Point out each malaria parasite.
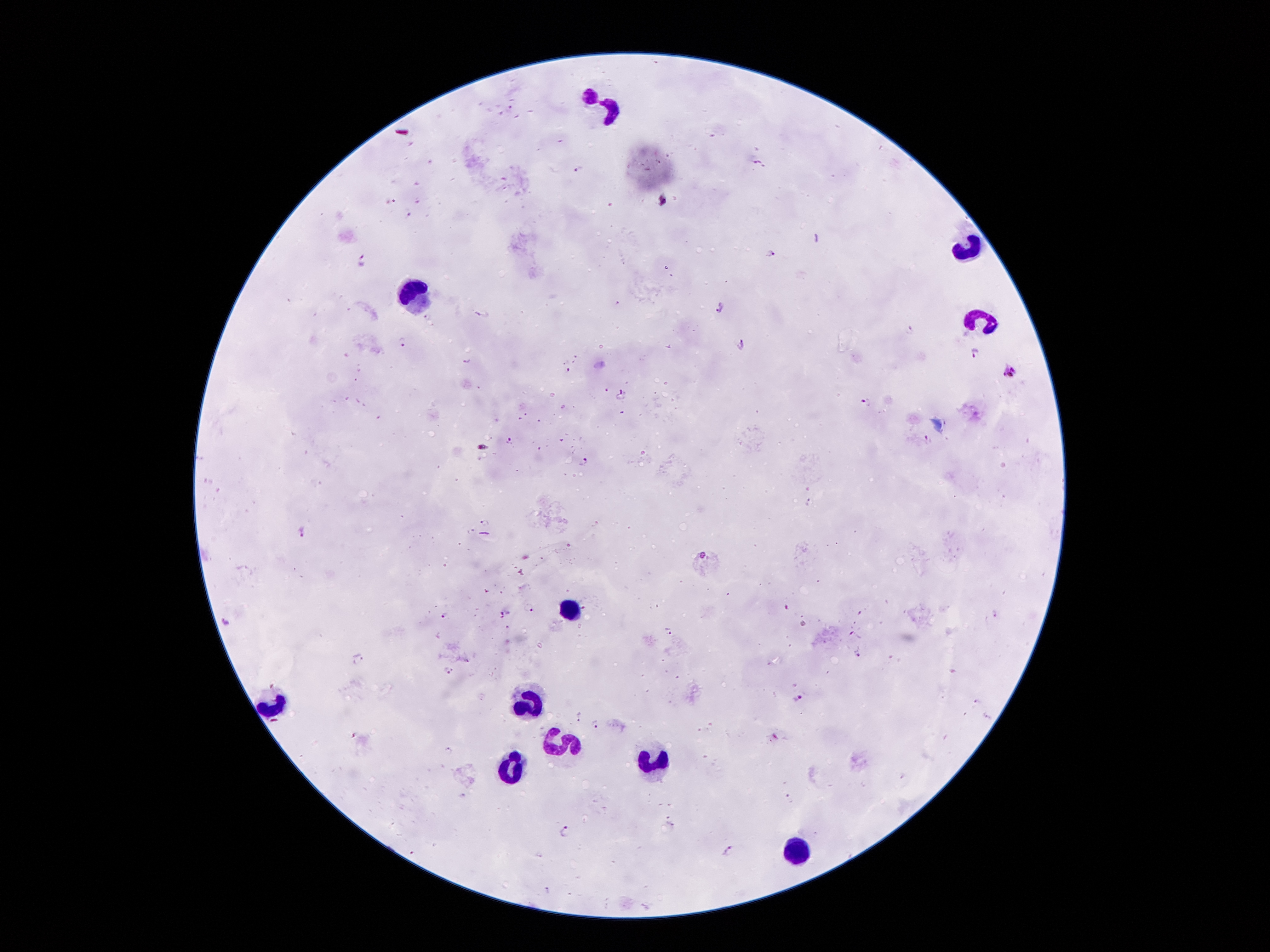
Approximate centers as (x, y) in pixels.
Malaria parasites: (578, 171), (664, 198), (410, 214), (772, 253), (362, 258), (617, 302), (722, 307), (482, 314), (429, 315), (910, 330), (404, 342), (741, 346), (972, 353), (468, 360), (1011, 369), (570, 370), (606, 391), (622, 395), (866, 400), (929, 441), (512, 442), (484, 448), (584, 462), (810, 502), (485, 522), (304, 530), (704, 554), (530, 608), (503, 613), (995, 613), (445, 615), (228, 623), (669, 631), (859, 652), (361, 661), (448, 672), (798, 697), (976, 701), (578, 716), (987, 717), (596, 724), (775, 737), (448, 751), (903, 777), (671, 824), (566, 828), (729, 850).

Summary:
  - Leukocyte locations: (604, 106), (967, 247), (417, 292), (980, 320), (565, 609), (530, 698), (269, 704), (563, 743), (656, 765), (509, 766), (792, 849)
  - Image size: 1270×952 pixels
  - Capture: smartphone through the microscope eyepiece
  - Preparation: thick blood film
  - Field of view: single
  - Magnification: 100x
  - Stain: Giemsa
  - Patient malaria status: infected with Plasmodium falciparum